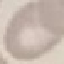
Summary:
  - Result: negative for malaria parasites
  - Image type: automatically extracted cell patch, resized to 64 × 64 pixels
  - Stain: Giemsa
  - Preparation: thin smear
  - Capture: smartphone through the microscope eyepiece